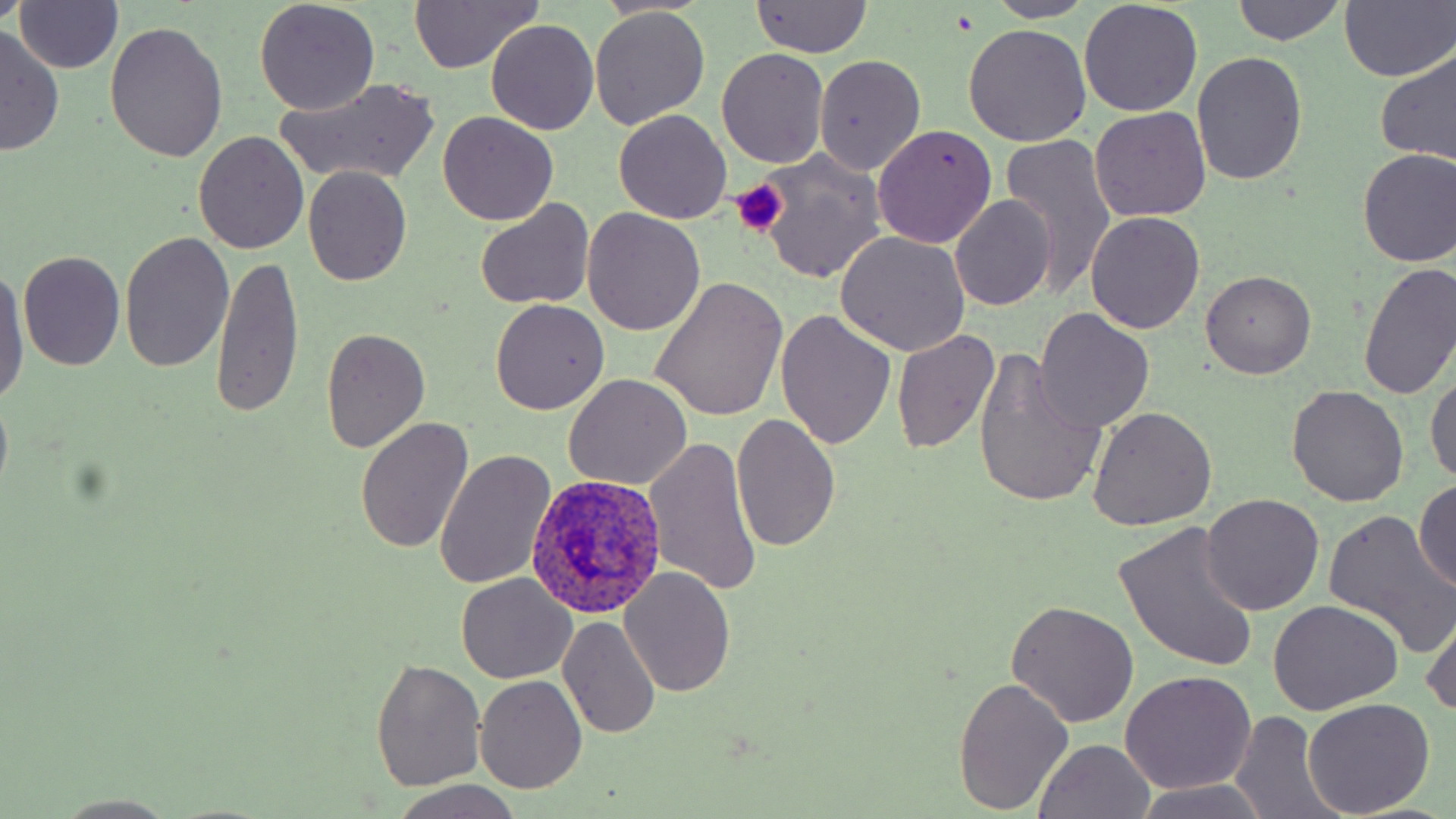

Summary:
  - Coordinate format: approximate bounding boxes as (x1, y1, x2, y2) in pixels
  - Plasmodium ovale-infected red blood cell locations: (526, 474, 669, 618)
  - Platelet locations: (730, 180, 786, 236)
  - Uninfected red blood cell locations: (591, 0, 713, 18), (748, 0, 872, 58), (987, 0, 1098, 22), (1231, 0, 1347, 46), (1340, 0, 1456, 82), (12, 1, 124, 73), (254, 1, 381, 114), (1079, 1, 1203, 116), (407, 2, 543, 73), (589, 8, 710, 130), (486, 20, 599, 135), (106, 21, 229, 163), (0, 24, 65, 156), (962, 24, 1093, 147), (1375, 44, 1456, 167), (717, 49, 829, 169), (1190, 52, 1306, 187), (815, 55, 925, 177), (276, 76, 441, 186), (1090, 106, 1212, 222), (614, 109, 731, 224), (438, 111, 559, 225), (873, 125, 997, 248), (193, 131, 310, 255), (1000, 134, 1119, 299), (1356, 148, 1456, 268), (748, 152, 886, 285), (303, 166, 412, 285), (951, 195, 1056, 310), (475, 199, 595, 310), (583, 209, 707, 336), (1087, 212, 1205, 333), (834, 231, 970, 356), (119, 232, 234, 373), (18, 250, 125, 370), (211, 255, 302, 420), (1359, 262, 1456, 401), (1, 263, 30, 408), (1201, 270, 1315, 378), (649, 275, 788, 419), (490, 300, 609, 415), (1034, 308, 1155, 435), (776, 310, 897, 450), (320, 327, 430, 453), (893, 330, 1000, 454), (974, 349, 1105, 513), (1427, 371, 1456, 486), (562, 375, 692, 492), (1285, 384, 1410, 508), (1088, 408, 1217, 531), (732, 414, 840, 552), (354, 418, 474, 556), (644, 436, 762, 599), (435, 448, 556, 589), (1413, 479, 1456, 591), (1201, 493, 1325, 616), (1323, 512, 1456, 659), (1113, 523, 1261, 672), (621, 569, 735, 696), (455, 573, 578, 684), (1268, 600, 1404, 714), (1006, 601, 1138, 727), (1420, 601, 1456, 724), (558, 614, 660, 738), (371, 658, 487, 792), (1121, 670, 1257, 794), (475, 674, 587, 794), (952, 676, 1074, 816), (1303, 698, 1436, 818), (1227, 710, 1338, 819), (1033, 739, 1158, 819), (389, 779, 524, 818), (1131, 780, 1274, 818), (56, 793, 176, 816)
  - Slide-level diagnosis: Plasmodium ovale
  - Magnification: 1000x
  - Field of view: single
  - Image size: 1456×819 pixels
  - Stain: May-Grünwald-Giemsa
  - Preparation: thin blood film
  - Modality: optical microscopy